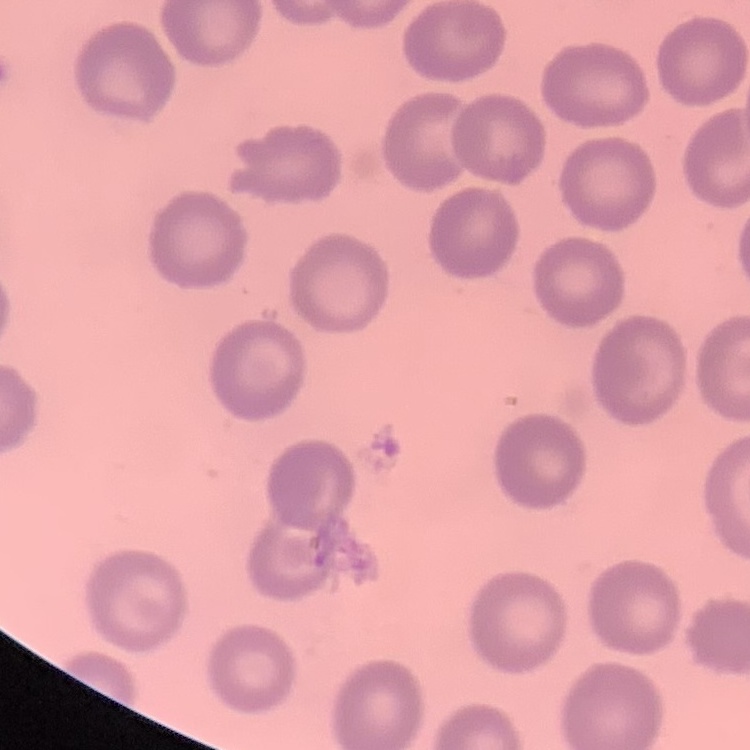 The red blood cells show no rouleaux formation. Field's or Giemsa stain. Thin blood film. Square crop of a larger photomicrograph.